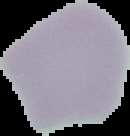

Summary:
  - Result: no Plasmodium parasites seen
  - Image type: segmented cell region with the area outside set to black
  - Image size: 130×136 pixels
  - Preparation: thin blood film